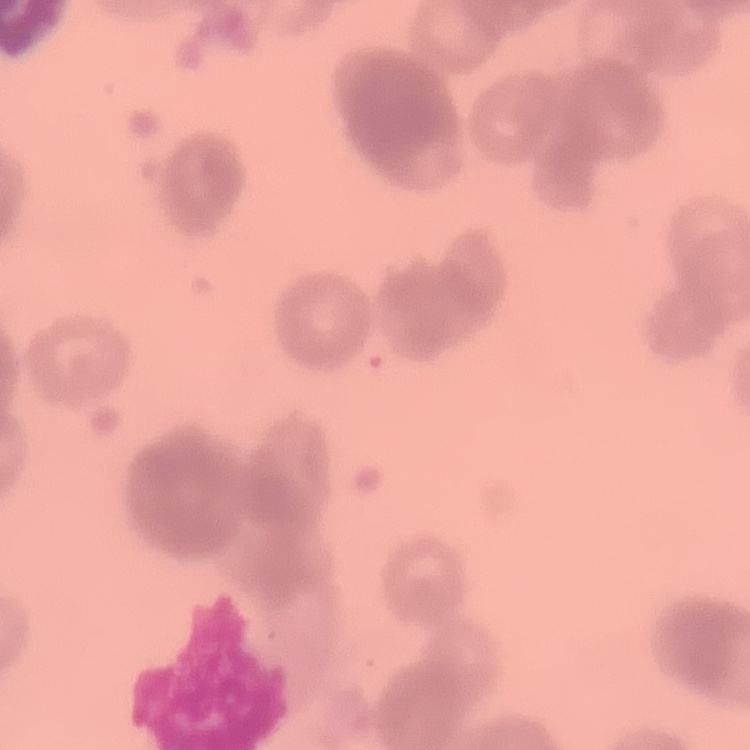

The erythrocytes show rouleaux formation. One tile cut from a larger photomicrograph. Stained with either Field's or Giemsa. Thin blood film.